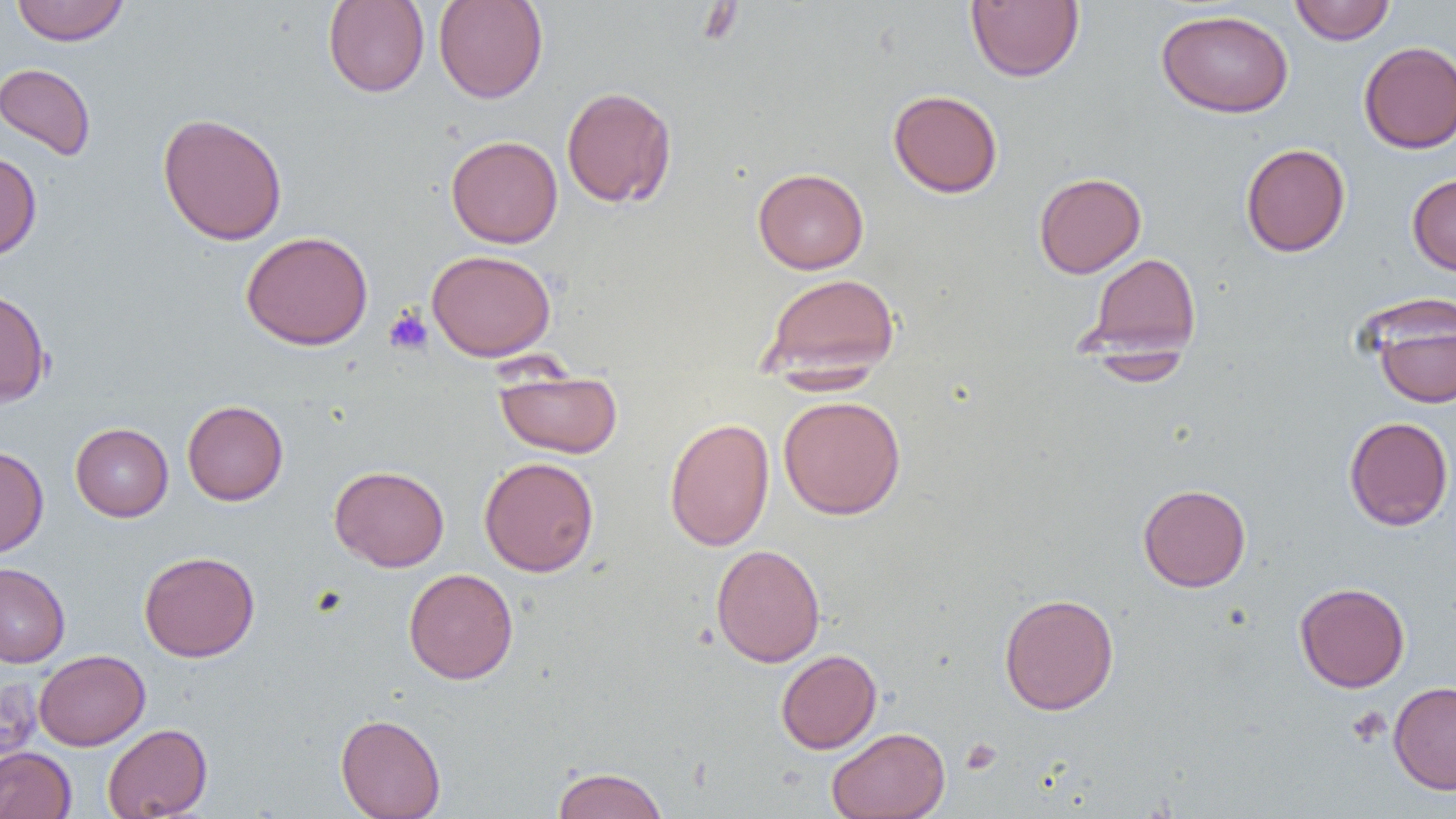

slide-level diagnosis = no evidence of blood parasites
uninfected red blood cell locations = approximate bounding boxes as [x1, y1, x2, y2] in pixels: [323, 0, 430, 97], [433, 0, 548, 104], [966, 0, 1084, 82], [1289, 0, 1396, 45], [11, 1, 129, 45], [1156, 8, 1293, 118], [1359, 41, 1456, 153], [0, 63, 97, 161], [561, 85, 677, 208], [888, 89, 1003, 198], [157, 112, 288, 245], [446, 135, 563, 248], [1241, 143, 1351, 257], [0, 151, 41, 260], [753, 167, 869, 274], [1033, 172, 1146, 278], [1407, 174, 1456, 276], [240, 231, 373, 350], [426, 249, 556, 361], [1085, 252, 1201, 359], [759, 272, 900, 380], [0, 287, 51, 407], [1368, 303, 1456, 408], [494, 369, 623, 459], [778, 395, 906, 520], [182, 400, 289, 505], [1343, 416, 1454, 531], [664, 417, 775, 552], [70, 423, 173, 521], [0, 445, 49, 557], [479, 457, 599, 577], [329, 465, 449, 572], [1138, 483, 1251, 592], [711, 544, 826, 667], [139, 551, 260, 662], [0, 562, 70, 667], [404, 568, 518, 685], [1294, 582, 1410, 692], [998, 592, 1119, 715], [34, 649, 150, 750], [776, 649, 882, 754], [0, 676, 43, 775], [1388, 680, 1456, 794], [335, 713, 446, 818], [102, 723, 212, 818], [826, 727, 950, 819], [0, 747, 77, 819], [552, 766, 668, 819]
preparation = thin blood film
magnification = 1000x
modality = optical microscopy
image size = 1456×819 pixels
platelet locations = approximate bounding boxes as [x1, y1, x2, y2] in pixels: [384, 306, 433, 355], [1347, 706, 1391, 748], [960, 738, 1002, 775]
field of view = single